Classify this cell by malaria status.
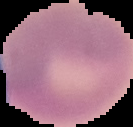

Uninfected.

Image is 133×127 pixels. Cell region segmented out of the field of view; the surrounding area is masked to black. From a thin blood film.